Name the parasite shown.
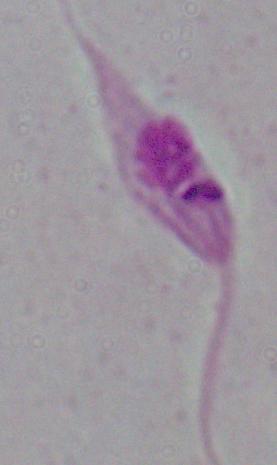
Leishmania.

Captured at 1000x magnification. Photomicrograph.